Comment on the background quality.
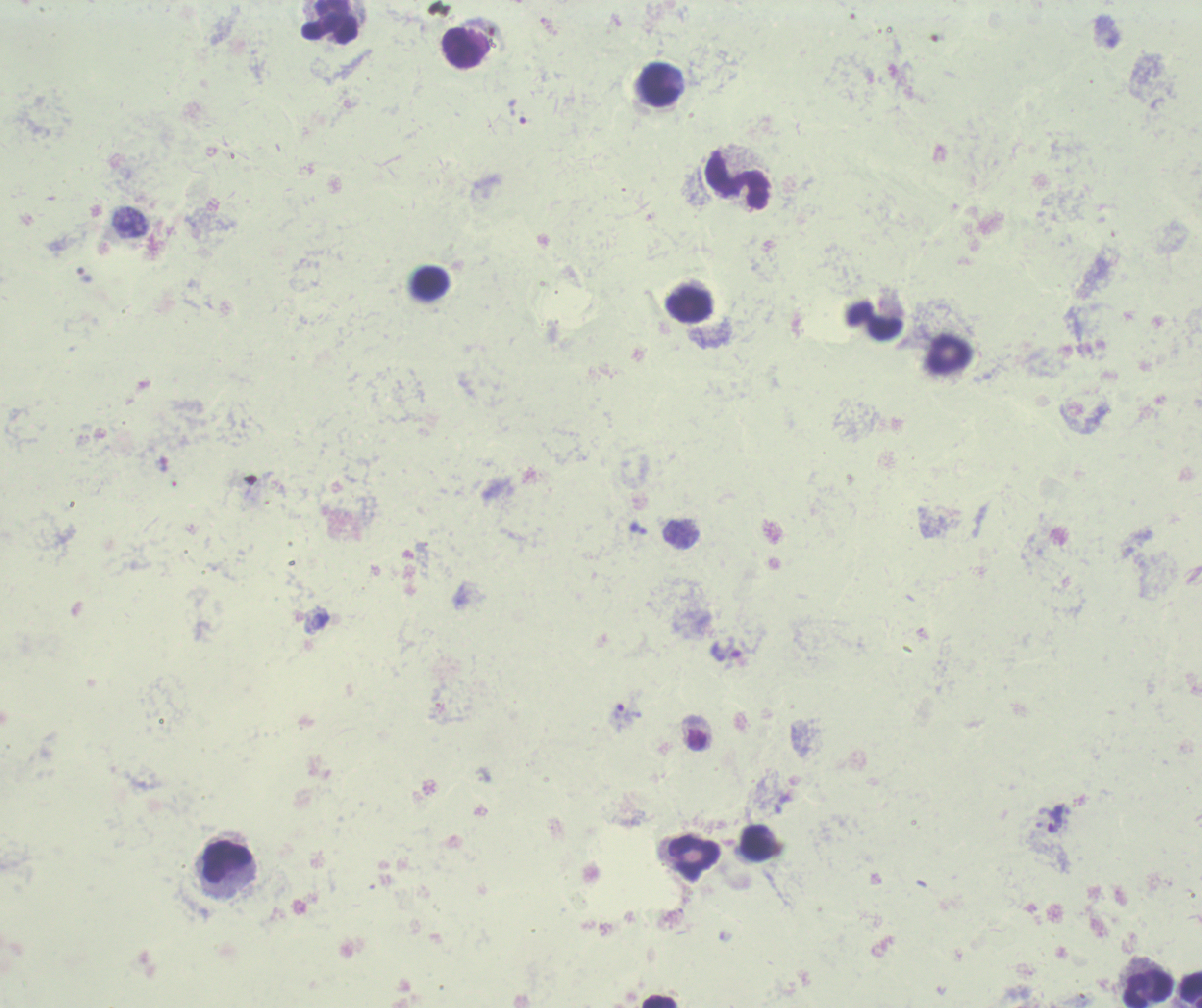
Poor.

Approximate object centers, in pixels from the top-left corner. Leukocyte locations: (x=329, y=22), (x=463, y=48), (x=659, y=84), (x=737, y=180), (x=430, y=282), (x=688, y=305), (x=875, y=321), (x=949, y=354), (x=757, y=843), (x=695, y=857), (x=228, y=861), (x=1190, y=989), (x=1148, y=990), (x=659, y=1001). Trophozoite locations: (x=517, y=111), (x=726, y=651), (x=626, y=717), (x=1051, y=819). Previously used in a real diagnosis. Romanowsky stain. Image is 1202×1008 pixels. Thick blood film. Captured at 100x magnification. Result: malaria parasites detected. Single field of view.